Classify this cell by malaria status.
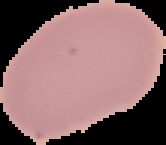

Uninfected.

{
  "image_size": "166×145 pixels",
  "image_type": "segmented cell region with the area outside set to black",
  "preparation": "thin blood smear"
}